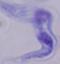 A trypanosome is shown. Micrograph. Captured at 1000x magnification.